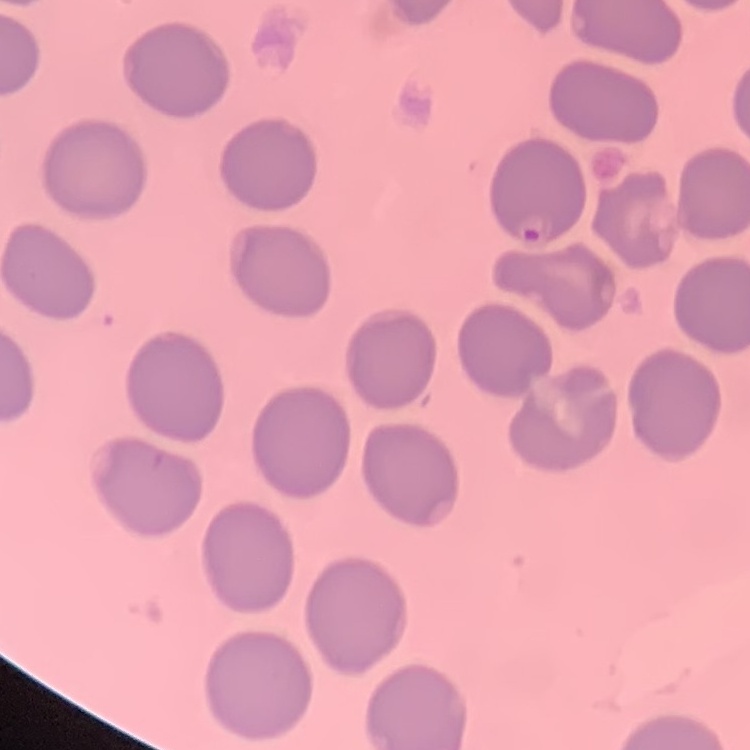

The red blood cells exhibit no rouleaux formation. Thin blood film. Field's or Giemsa stain. One tile cut from a larger photomicrograph.